Give the position of every Plasmodium parasite.
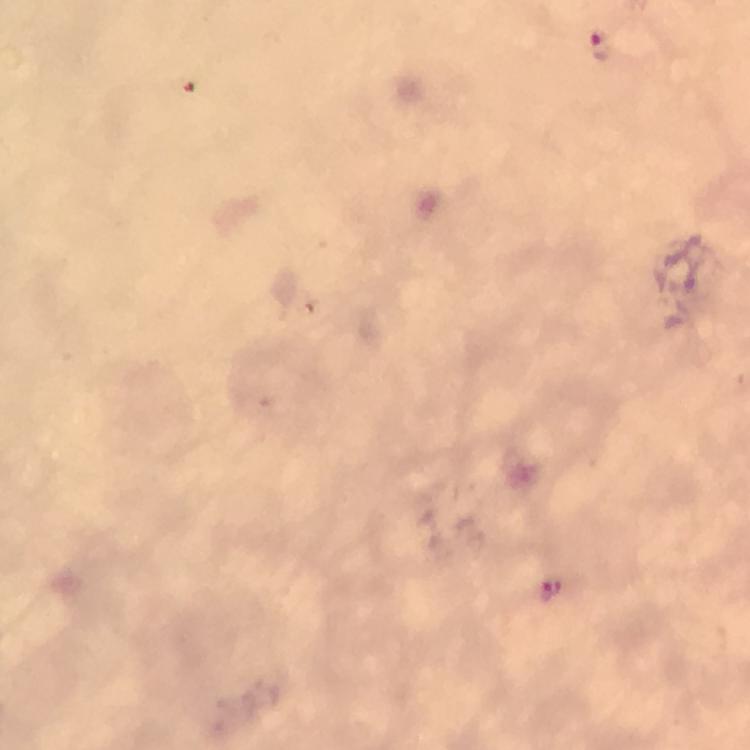
Approximate object centers, in pixels from the top-left corner.
Plasmodium parasites: (x=550, y=591).

Summary:
  - Preparation: thick blood smear
  - Magnification: 100x
  - Context: from a malaria diagnostic workup
  - Image size: 750×750 pixels
  - Capture: smartphone mounted on the microscope
  - Stain: Giemsa
  - Cropped from: one field of view
  - Immersion oil: applied